Outline each uninfected red blood cell.
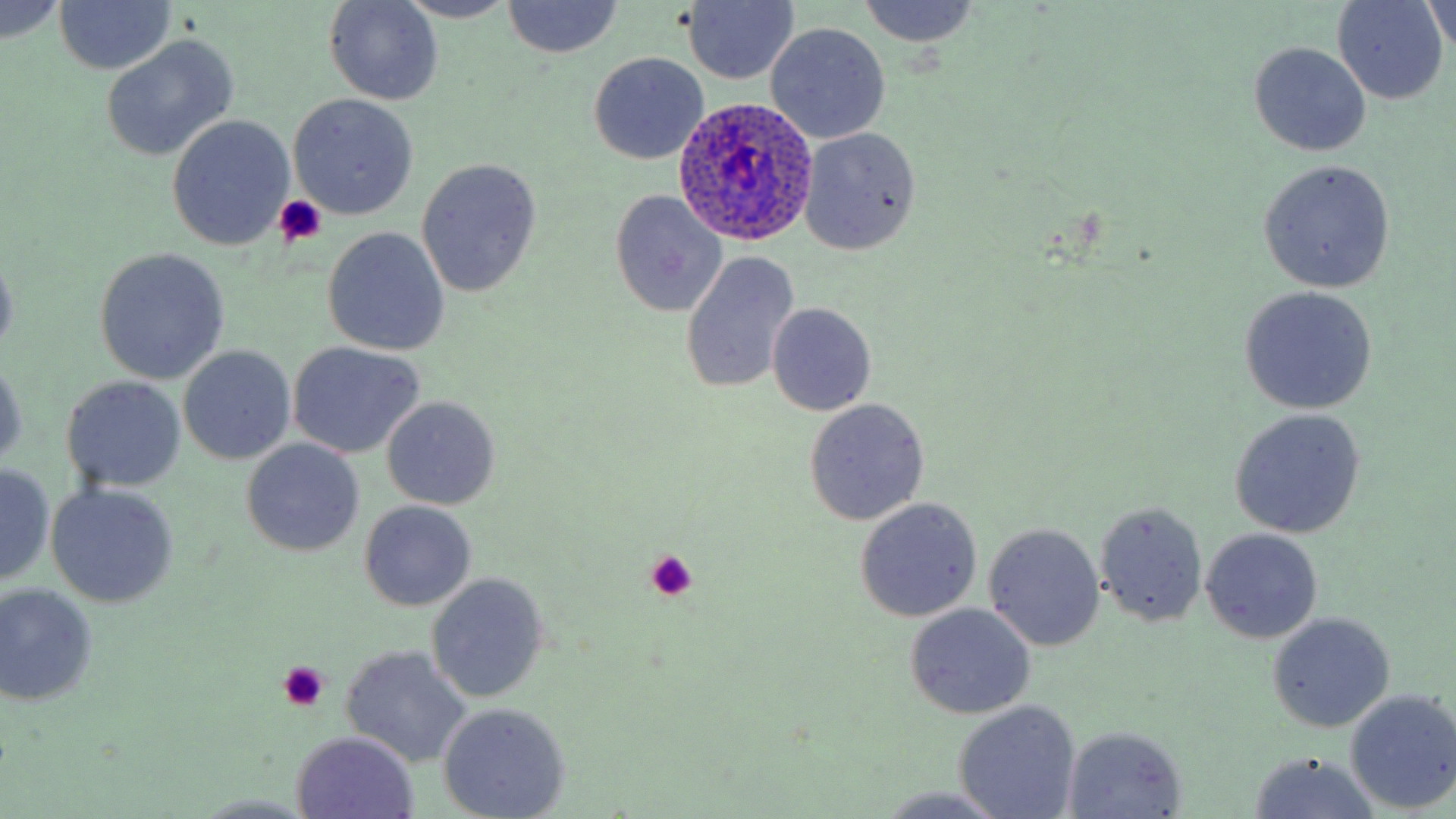
Approximate bounding boxes as (x1, y1, x2, y2) in pixels.
Uninfected red blood cells: (53, 0, 175, 74), (324, 0, 443, 105), (857, 0, 982, 49), (1334, 0, 1449, 104), (395, 1, 521, 23), (681, 1, 800, 85), (0, 2, 66, 44), (501, 2, 624, 58), (1423, 2, 1453, 55), (765, 23, 890, 144), (102, 36, 238, 161), (1249, 42, 1371, 157), (588, 52, 707, 165), (289, 93, 419, 220), (167, 115, 295, 250), (799, 127, 922, 255), (415, 159, 542, 298), (1258, 160, 1396, 292), (609, 190, 726, 317), (322, 227, 451, 356), (0, 248, 19, 361), (94, 249, 229, 384), (680, 251, 800, 395), (1239, 286, 1378, 414), (766, 302, 877, 415), (287, 341, 424, 459), (178, 345, 297, 465), (1, 357, 27, 471), (61, 376, 188, 494), (382, 397, 499, 509), (804, 399, 930, 525), (1229, 408, 1366, 539), (241, 439, 365, 556), (0, 463, 54, 586), (47, 483, 178, 608), (854, 497, 983, 622), (1096, 499, 1208, 628), (359, 500, 477, 610), (983, 523, 1105, 651), (1200, 528, 1324, 644), (426, 573, 550, 703), (0, 583, 99, 709), (905, 604, 1036, 719), (1267, 612, 1394, 732), (339, 645, 474, 768), (1345, 689, 1456, 813), (953, 700, 1082, 819), (437, 703, 572, 819), (1062, 727, 1188, 817), (291, 732, 419, 817), (1244, 752, 1382, 818), (877, 786, 1010, 819), (191, 793, 322, 817).

Summary:
  - Platelet locations: (273, 194, 326, 245), (644, 550, 699, 602), (278, 661, 330, 710)
  - Plasmodium ovale-infected red blood cell locations: (672, 95, 818, 247)
  - Slide-level diagnosis: Plasmodium ovale
  - Stain: May-Grünwald-Giemsa
  - Modality: light microscopy
  - Magnification: 1000x
  - Preparation: thin blood smear
  - Field of view: one of a larger specimen
  - Image size: 1456×819 pixels